Assess this cell for malaria.
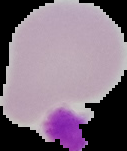

It is uninfected.

Summary:
  - Preparation: thin blood smear
  - Image size: 127×151 pixels
  - Image type: cell region segmented out of the field of view; surrounding area masked to black